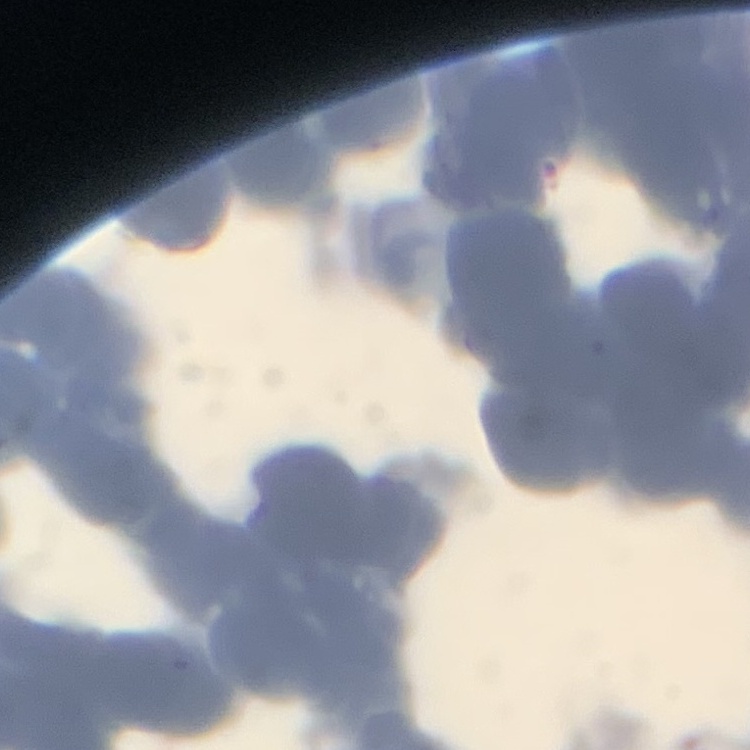
The erythrocytes show rouleaux formation. Stained with either Field's or Giemsa. Thin blood film. One tile cut from a larger photomicrograph.